Name the parasite shown.
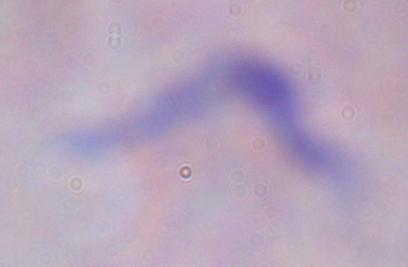

A trypanosome.

1000x magnification. Photomicrograph.